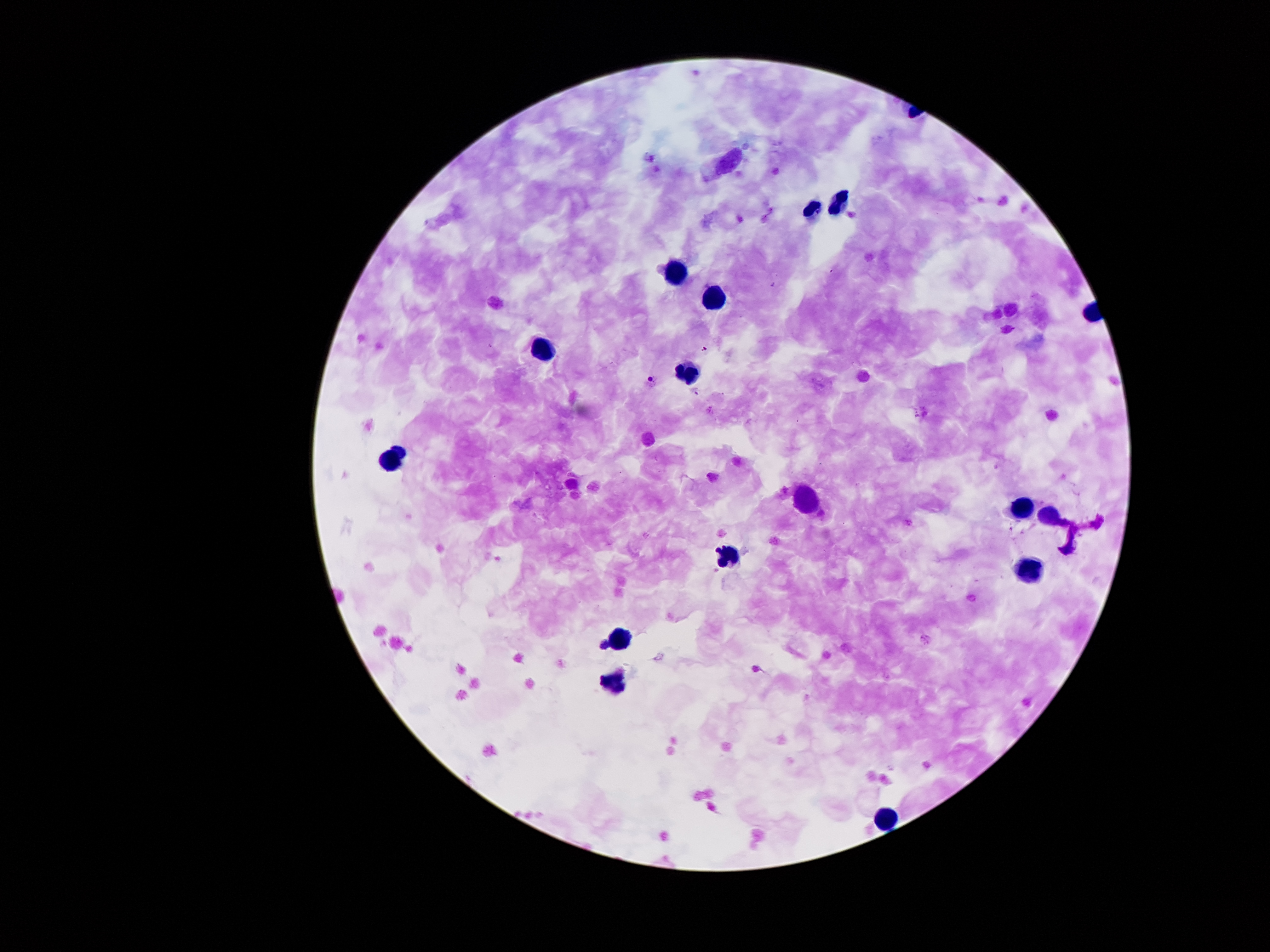

coordinate format = approximate centers as {x, y} in pixels
malaria parasite locations = {704, 349}, {696, 391}, {1012, 529}, {972, 598}
leukocyte locations = {727, 161}, {838, 203}, {813, 213}, {675, 275}, {711, 295}, {544, 346}, {689, 373}, {389, 461}, {804, 502}, {1023, 509}, {1048, 514}, {729, 557}, {1030, 568}, {620, 637}, {613, 681}, {887, 819}
field of view = single
magnification = 100x
preparation = thick blood smear
image size = 1270×952 pixels
patient malaria status = infected with Plasmodium falciparum
capture = smartphone camera through the microscope eyepiece
stain = Giemsa